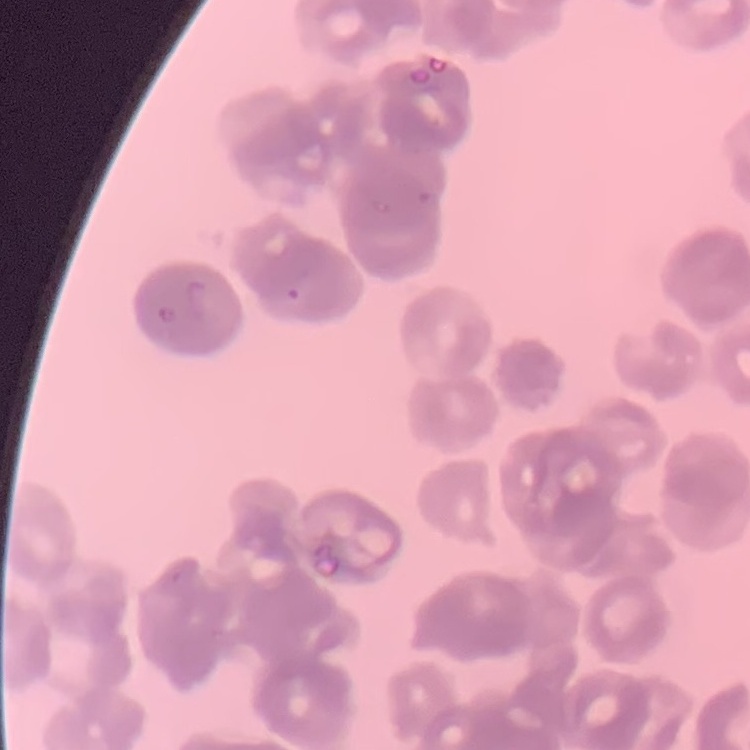
Summary:
  - Red blood cell morphology: rouleaux formation
  - Stain: Field's or Giemsa
  - Image type: square crop of a larger photomicrograph
  - Preparation: thin blood film